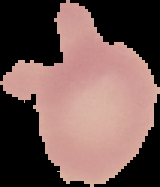

Summary:
  - Image size: 160×187 pixels
  - Image type: segmented cell region with the area outside set to black
  - Result: no malaria parasites seen
  - Preparation: thin blood smear